Give the extent of all uninfected red blood cells.
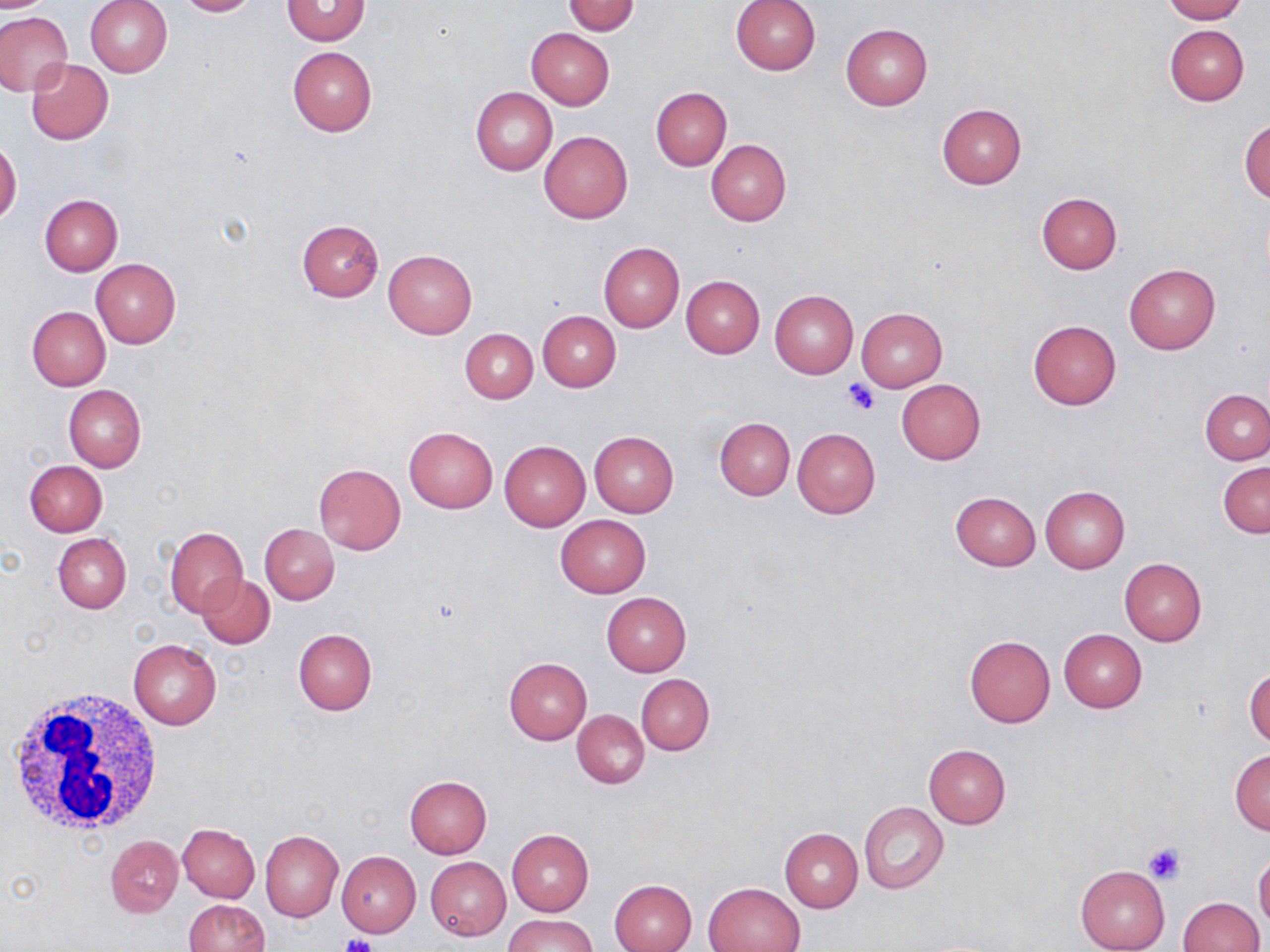

Approximate bounding boxes as (x1,y1)-(x2,y2) corner pairs in pixels.
Uninfected red blood cells: (0,0)-(57,13), (86,0)-(172,77), (173,0)-(259,17), (730,0)-(821,75), (1162,0)-(1247,23), (282,1)-(369,45), (563,1)-(640,36), (0,11)-(72,96), (841,24)-(933,109), (1165,24)-(1249,106), (527,28)-(614,110), (287,46)-(377,136), (26,58)-(113,144), (651,87)-(731,172), (470,88)-(556,175), (937,105)-(1026,189), (1240,120)-(1270,201), (539,131)-(633,223), (0,140)-(21,225), (706,140)-(791,226), (1036,193)-(1122,274), (40,194)-(123,275), (295,219)-(384,301), (599,242)-(684,332), (384,249)-(477,339), (90,258)-(181,348), (1124,264)-(1220,353), (681,275)-(765,358), (770,289)-(858,378), (27,307)-(110,390), (856,308)-(948,390), (537,310)-(620,391), (1028,320)-(1122,410), (460,328)-(537,404), (896,379)-(986,464), (63,385)-(146,472), (1201,389)-(1270,464), (715,417)-(795,500), (404,426)-(497,513), (792,428)-(880,518), (589,430)-(679,517), (499,440)-(590,531), (24,460)-(108,536), (1217,462)-(1269,539), (314,463)-(406,554), (1040,486)-(1129,572), (950,492)-(1041,571), (556,515)-(650,596), (260,524)-(338,605), (165,526)-(248,615), (53,534)-(131,613), (1119,557)-(1207,645), (197,573)-(274,649), (602,592)-(691,675), (293,628)-(377,714), (1058,629)-(1147,712), (965,635)-(1056,728), (129,639)-(221,729), (503,657)-(592,745), (1246,666)-(1269,748), (636,674)-(714,756), (573,710)-(649,788), (924,745)-(1010,828), (1229,750)-(1270,834), (404,775)-(492,858), (858,801)-(949,894), (177,823)-(259,902), (780,827)-(862,911), (507,829)-(594,917), (260,830)-(344,922), (106,835)-(182,917), (337,850)-(420,937), (1254,851)-(1270,932), (425,857)-(511,940), (1075,865)-(1169,952), (610,879)-(697,952), (703,882)-(806,951), (1176,897)-(1264,952), (184,899)-(269,951), (503,913)-(598,952).

White blood cell locations: (8,686)-(168,839). Platelet locations: (843,380)-(879,416), (1144,842)-(1187,885), (341,935)-(378,952). Slide-level diagnosis: no evidence of blood parasites. Image is 1270×952 pixels. Thin blood smear. Captured at 1000x magnification. Single field of view. May-Grünwald-Giemsa-stained preparation. Optical microscopy.